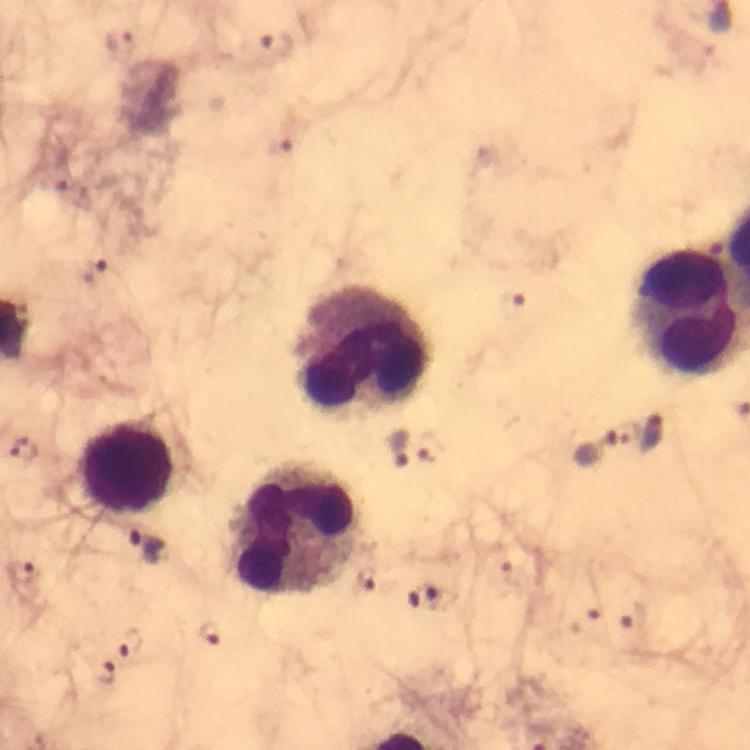

Approximate centers as [x, y] in pixels.
Summary:
  - Plasmodium parasite locations: [274, 47], [94, 271], [399, 447], [594, 447], [25, 452], [145, 547], [20, 574], [211, 632], [130, 644], [104, 672]
  - Leukocyte locations: [365, 348], [128, 466], [297, 530]
  - Immersion oil: applied
  - Magnification: 100x
  - Context: from a malaria diagnostic workup
  - Stain: Giemsa
  - Capture: smartphone camera through the microscope
  - Image size: 750×750 pixels
  - Cropped from: a single field of view
  - Preparation: thick blood smear